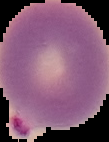
Summary:
  - Preparation: thin blood smear
  - Image size: 109×142 pixels
  - Image type: cell region segmented out of the field of view; surrounding area masked to black
  - Result: malaria parasites detected